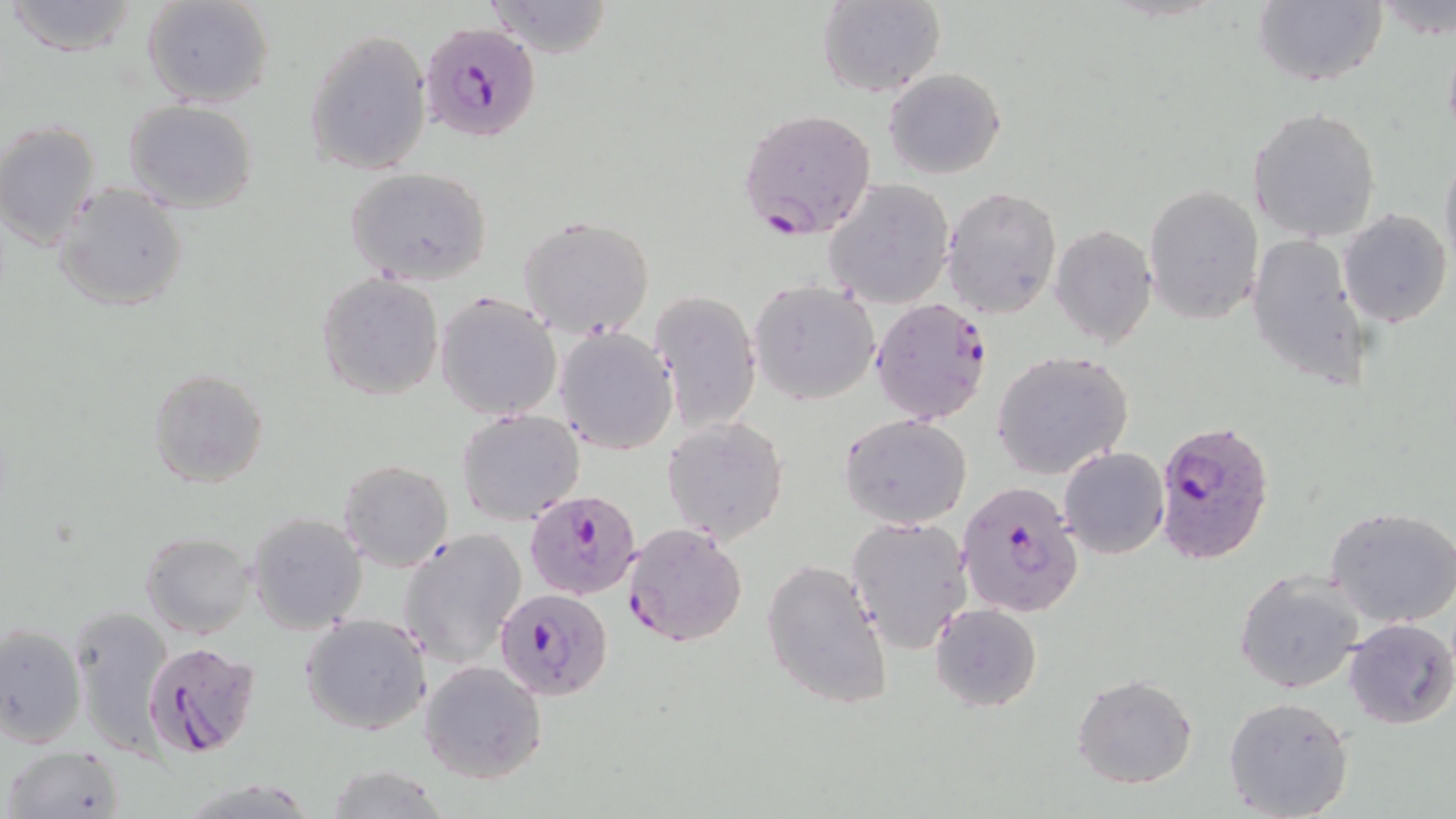
Approximate bounding boxes as (x1, y1, x2, y2) in pixels. Uninfected red blood cell locations: (4, 0, 143, 56), (142, 0, 274, 108), (815, 0, 944, 98), (1252, 0, 1388, 89), (483, 1, 616, 58), (1376, 2, 1456, 41), (304, 27, 433, 177), (884, 67, 1005, 179), (123, 101, 259, 213), (1248, 106, 1381, 244), (0, 121, 101, 249), (1439, 145, 1456, 275), (344, 167, 493, 286), (827, 178, 957, 308), (52, 183, 189, 312), (1145, 184, 1263, 325), (943, 186, 1063, 319), (1339, 208, 1452, 329), (517, 214, 657, 339), (1050, 225, 1156, 348), (1246, 232, 1374, 388), (316, 273, 442, 399), (748, 280, 879, 404), (648, 289, 762, 433), (434, 292, 563, 423), (554, 328, 678, 454), (992, 350, 1134, 479), (148, 368, 270, 489), (456, 409, 585, 526), (839, 414, 972, 530), (662, 416, 789, 544), (1058, 446, 1169, 559), (337, 459, 453, 571), (1325, 505, 1456, 627), (249, 513, 368, 634), (846, 516, 971, 653), (398, 529, 527, 669), (140, 533, 255, 638), (761, 559, 892, 708), (1233, 566, 1366, 697), (68, 604, 173, 749), (929, 604, 1042, 713), (300, 613, 432, 735), (1342, 617, 1455, 730), (0, 623, 87, 749), (419, 659, 546, 784), (1072, 673, 1199, 788), (1223, 695, 1354, 818), (3, 744, 126, 819), (319, 765, 454, 819). Plasmodium falciparum-infected red blood cell locations: (422, 20, 542, 141), (738, 108, 878, 239), (870, 299, 994, 424), (1153, 418, 1276, 566), (956, 479, 1085, 619), (525, 489, 643, 600), (622, 522, 748, 647), (493, 585, 613, 700), (143, 641, 263, 758). Slide-level diagnosis: Plasmodium falciparum. 1000x magnification. Thin blood film. May-Grünwald-Giemsa stain. One field of a larger specimen. Image is 1456×819 pixels. Light microscopy.